Give the position of every malaria parasite.
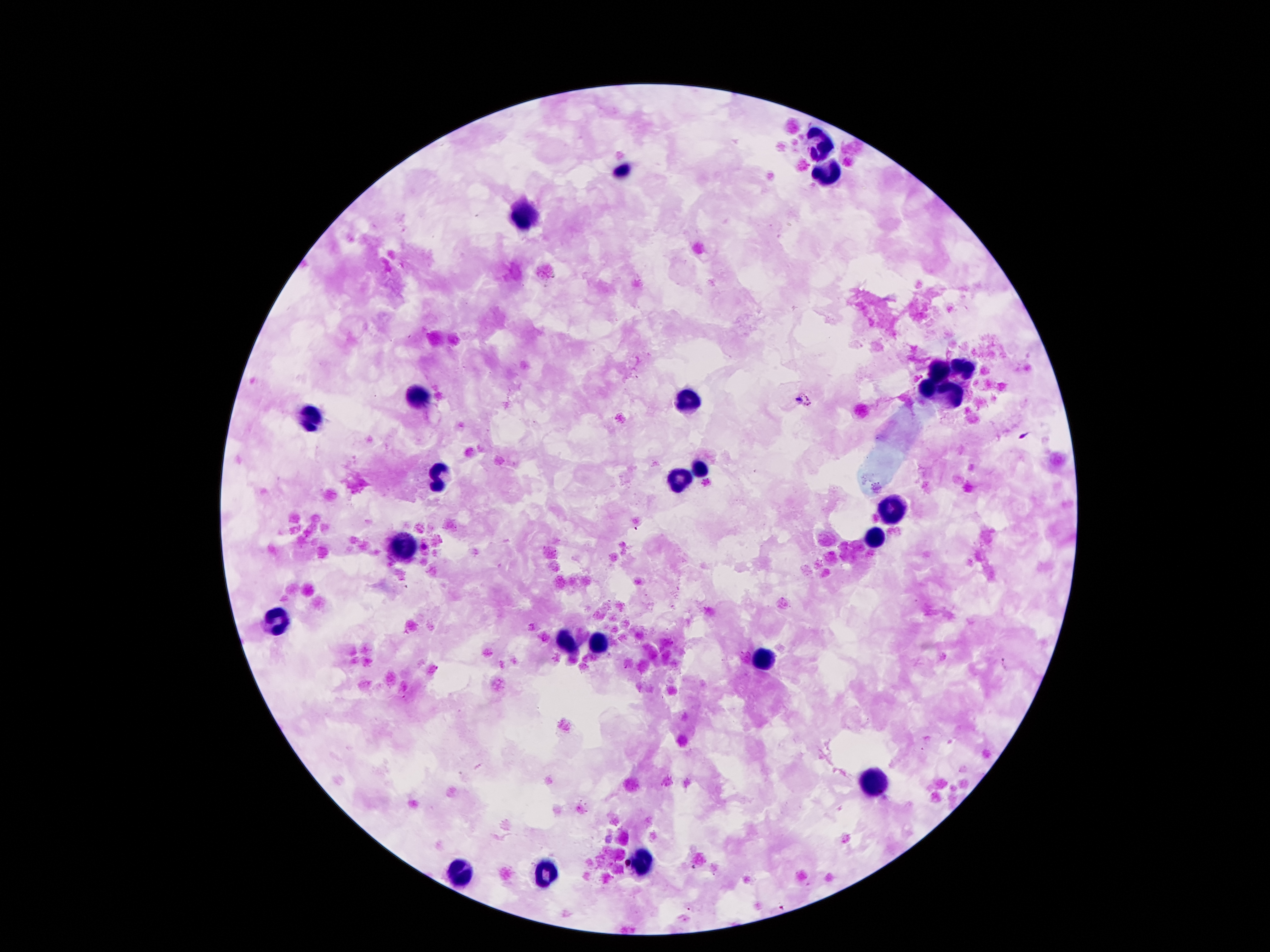
Approximate centers as {x, y} in pixels.
Malaria parasites: {809, 396}, {1025, 437}, {1005, 665}, {782, 907}.

leukocyte locations = {822, 145}, {623, 170}, {824, 170}, {517, 216}, {940, 369}, {964, 369}, {926, 391}, {420, 396}, {954, 399}, {688, 402}, {315, 415}, {700, 468}, {436, 475}, {677, 478}, {891, 506}, {875, 539}, {400, 545}, {278, 618}, {567, 643}, {598, 643}, {763, 656}, {875, 786}, {637, 862}, {460, 870}, {547, 870}
patient malaria status = positive for Plasmodium falciparum
preparation = thick blood film
capture = smartphone camera through the microscope eyepiece
image size = 1270×952 pixels
field of view = one from this slide
stain = Giemsa
magnification = 100x